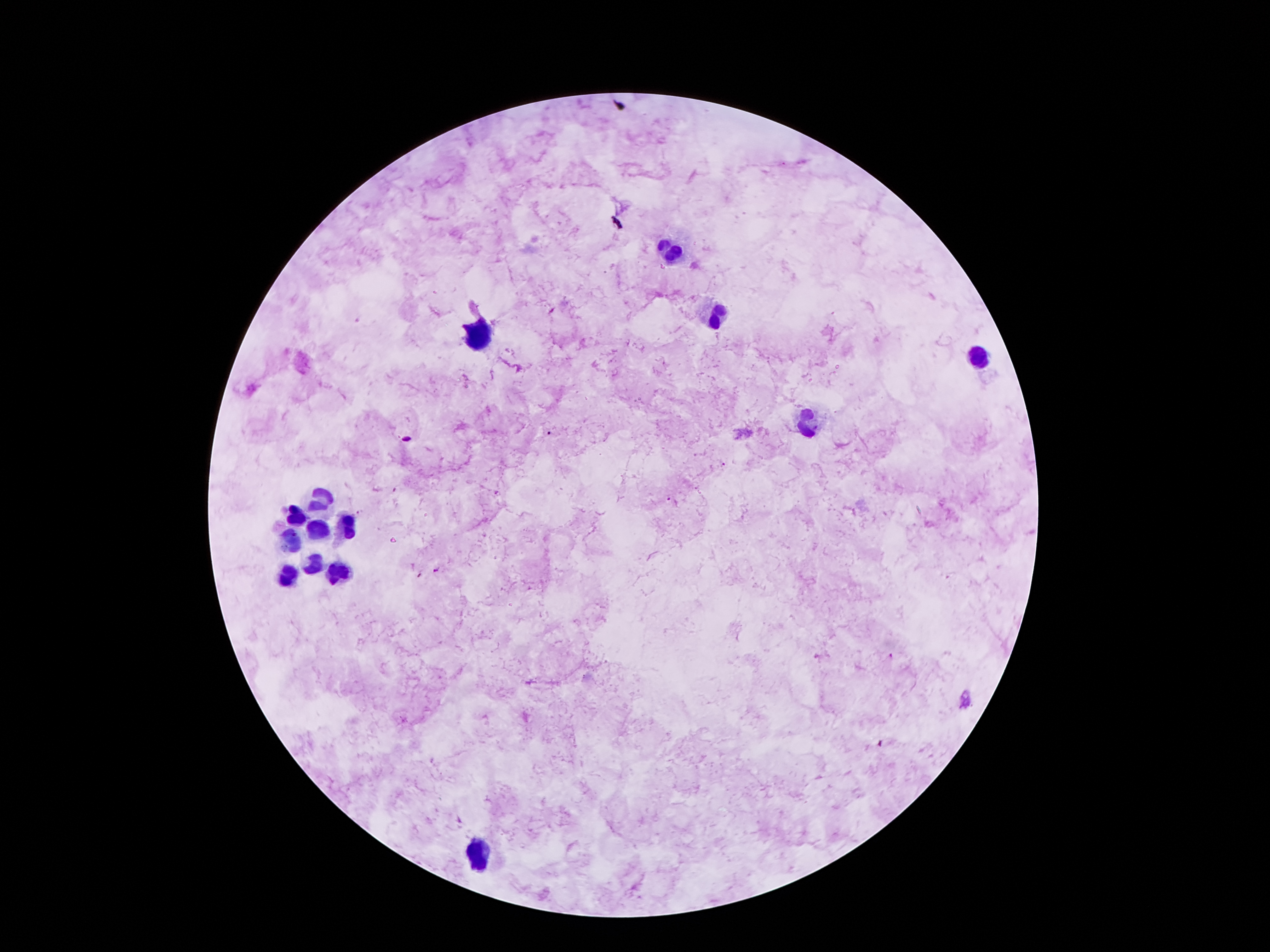

patient_malaria_status: positive for Plasmodium falciparum
image_size: 1270×952 pixels
stain: Giemsa
preparation: thick blood smear
plasmodium_parasite_locations: 'approximate centers as [x, y] in pixels: [550, 433], [723, 465], [668, 498], [434, 569], [890, 655]'
leukocyte_locations: 'approximate centers as [x, y] in pixels: [668, 251], [712, 316], [477, 335], [977, 358], [813, 423], [318, 499], [295, 518], [349, 528], [313, 531], [288, 541], [313, 564], [337, 571], [290, 577], [479, 854]'
magnification: 100x
field_of_view: one from this slide
capture: smartphone camera through the microscope eyepiece